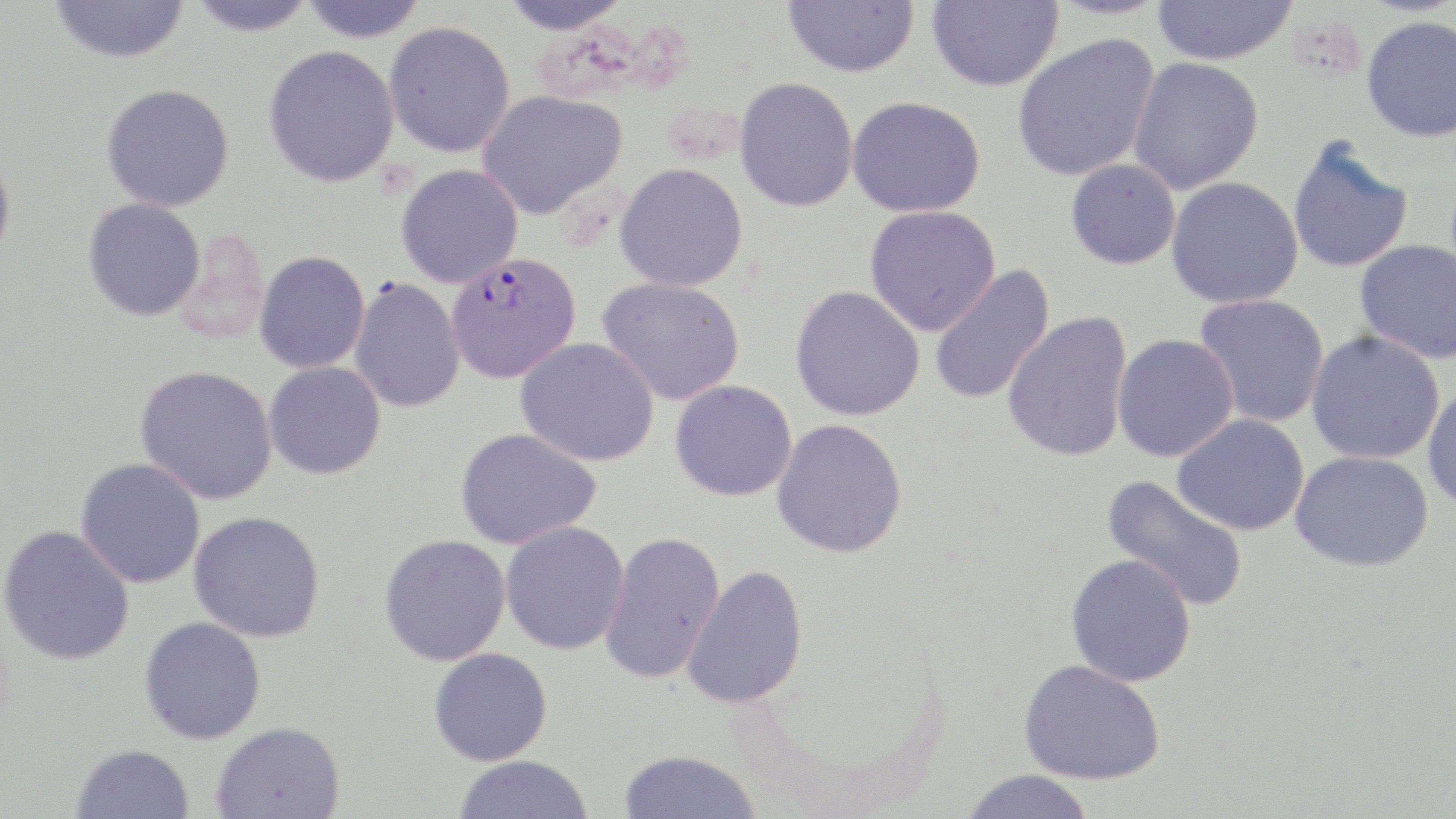

Plasmodium falciparum-infected red blood cell locations = approximate bounding boxes as [x1, y1, x2, y2] in pixels: [446, 251, 582, 384]
slide-level diagnosis = Plasmodium falciparum
modality = light microscopy
preparation = thin blood film
magnification = 1000x
image size = 1456×819 pixels
field of view = single
uninfected red blood cell locations = approximate bounding boxes as [x1, y1, x2, y2] in pixels: [50, 0, 189, 65], [186, 0, 318, 37], [299, 0, 428, 42], [497, 0, 634, 35], [783, 0, 919, 78], [1045, 0, 1172, 20], [1150, 0, 1299, 66], [926, 1, 1063, 91], [1361, 15, 1456, 142], [383, 21, 515, 158], [1012, 35, 1159, 181], [263, 45, 400, 187], [1127, 56, 1264, 193], [734, 77, 858, 212], [101, 84, 235, 212], [477, 90, 627, 220], [847, 96, 985, 218], [1286, 138, 1414, 275], [0, 146, 15, 269], [1065, 159, 1181, 270], [614, 163, 748, 292], [395, 164, 523, 288], [1166, 176, 1303, 309], [83, 197, 206, 322], [865, 205, 1001, 335], [1354, 240, 1456, 364], [254, 251, 370, 374], [928, 265, 1056, 405], [596, 277, 745, 406], [349, 278, 465, 413], [790, 285, 925, 421], [1194, 293, 1330, 427], [1002, 311, 1133, 462], [1306, 330, 1446, 464], [1112, 333, 1239, 462], [515, 338, 660, 466], [263, 361, 386, 480], [135, 365, 278, 505], [670, 380, 798, 502], [1422, 384, 1456, 513], [1173, 413, 1310, 536], [771, 419, 907, 558], [455, 428, 601, 549], [1290, 450, 1434, 571], [75, 458, 206, 589], [1102, 475, 1249, 611], [188, 511, 325, 642], [500, 522, 629, 655], [0, 525, 135, 666], [599, 531, 725, 684], [379, 534, 511, 666], [1066, 554, 1196, 687], [682, 564, 808, 710], [139, 617, 266, 744], [429, 648, 552, 766], [1019, 659, 1165, 784], [211, 721, 345, 818], [71, 744, 194, 819], [619, 749, 762, 819], [454, 755, 593, 818], [960, 769, 1096, 819]
stain = May-Grünwald-Giemsa